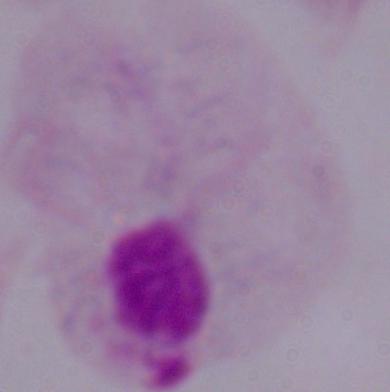
magnification: 1000x
identification: trichomonad
modality: photomicrograph